Identify the cell.
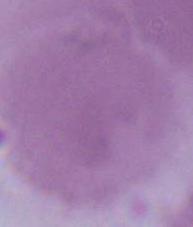

An erythrocyte.

1000x magnification. Photomicrograph.